Comment on the morphology of the red blood cells.
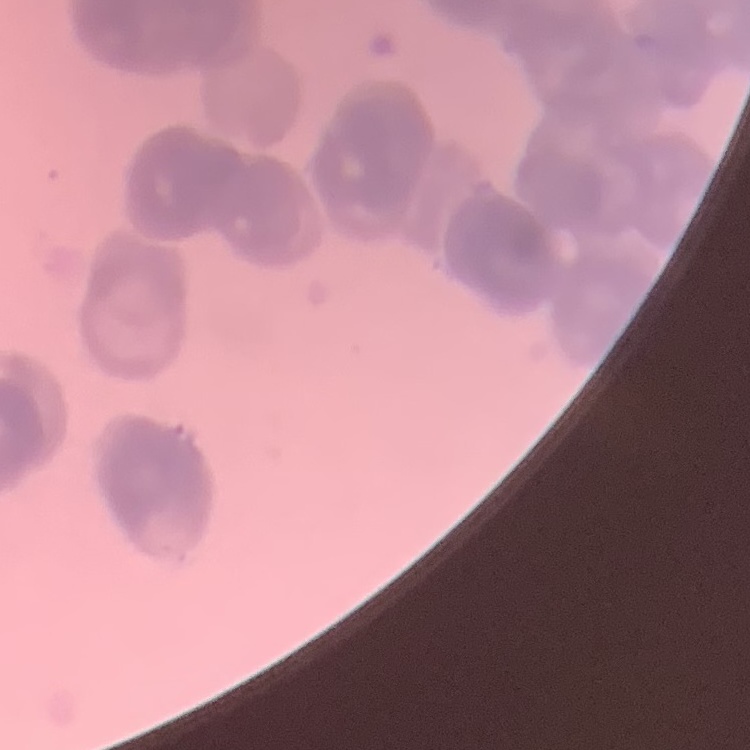

Rouleaux formation.

preparation: thin blood film
stain: Field's or Giemsa
image_type: square crop of a larger photomicrograph